Name the parasite shown.
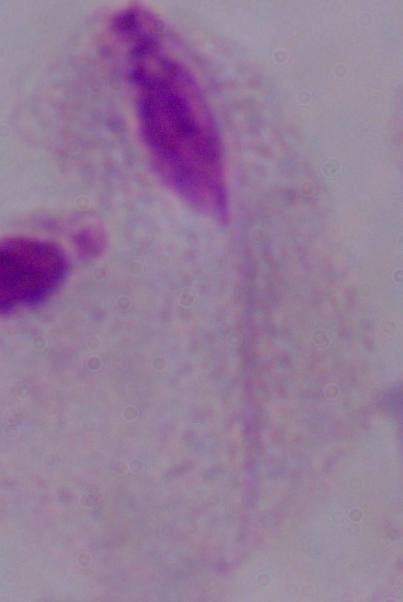
A trichomonad.

Summary:
  - Magnification: 1000x
  - Modality: micrograph